Locate platelets.
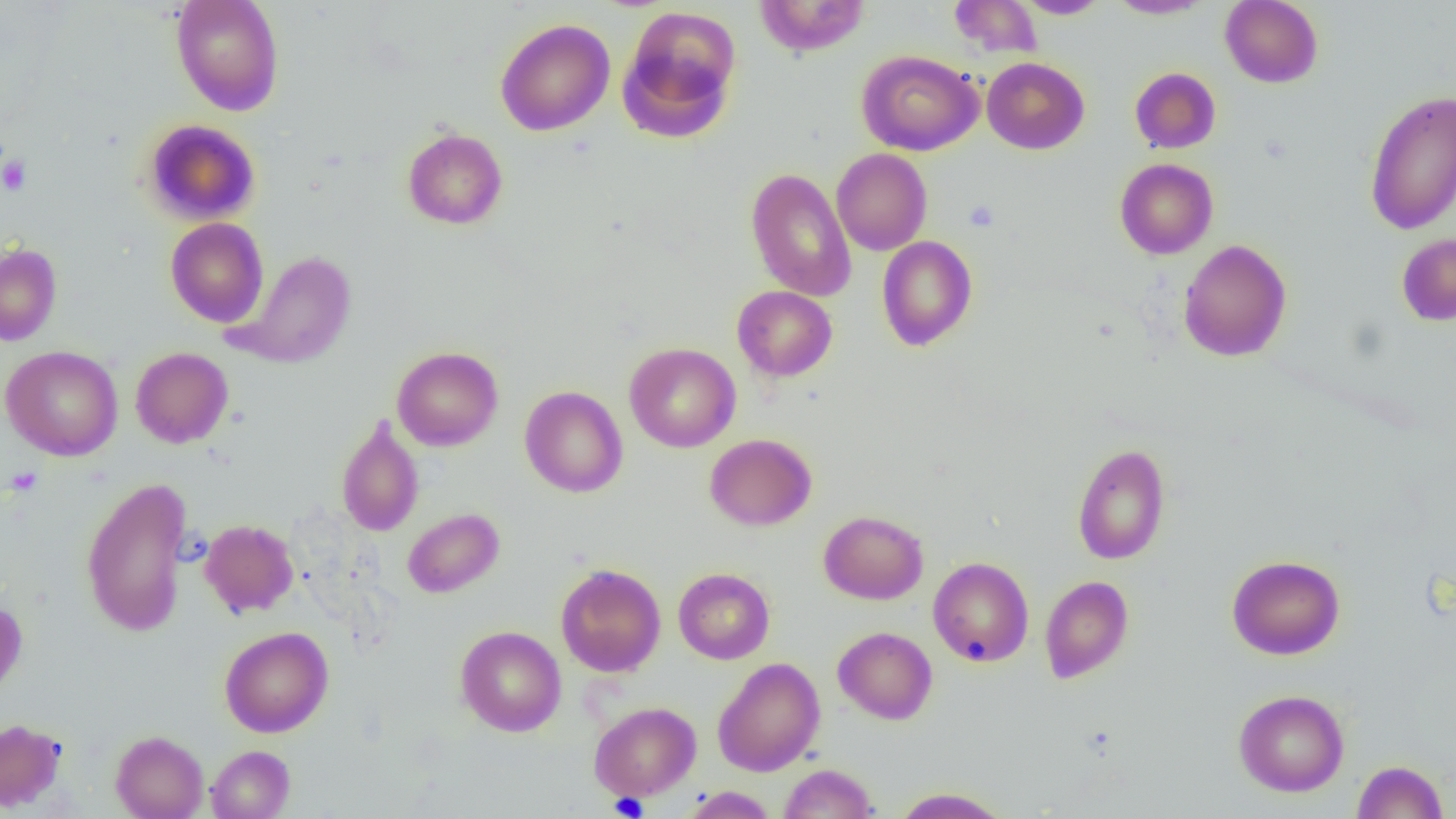

Approximate bounding boxes as named x1/y1/x2/y2 corners in pixels.
Platelets: (x1=0, y1=155, x2=31, y2=196), (x1=964, y1=200, x2=1000, y2=231), (x1=4, y1=466, x2=43, y2=496), (x1=610, y1=792, x2=649, y2=818).

Uninfected red blood cell locations: (x1=171, y1=0, x2=285, y2=116), (x1=755, y1=0, x2=870, y2=56), (x1=949, y1=0, x2=1043, y2=58), (x1=1106, y1=0, x2=1211, y2=19), (x1=1220, y1=0, x2=1323, y2=88), (x1=1015, y1=1, x2=1110, y2=18), (x1=618, y1=6, x2=743, y2=144), (x1=495, y1=18, x2=615, y2=136), (x1=856, y1=50, x2=983, y2=155), (x1=982, y1=57, x2=1089, y2=154), (x1=1130, y1=67, x2=1221, y2=153), (x1=1364, y1=89, x2=1456, y2=235), (x1=142, y1=118, x2=260, y2=225), (x1=402, y1=128, x2=508, y2=230), (x1=831, y1=148, x2=932, y2=255), (x1=1115, y1=158, x2=1218, y2=259), (x1=745, y1=167, x2=857, y2=302), (x1=165, y1=217, x2=269, y2=327), (x1=1397, y1=233, x2=1456, y2=325), (x1=877, y1=235, x2=978, y2=352), (x1=1178, y1=239, x2=1292, y2=362), (x1=0, y1=243, x2=62, y2=346), (x1=232, y1=250, x2=357, y2=369), (x1=732, y1=286, x2=837, y2=382), (x1=624, y1=342, x2=740, y2=452), (x1=1, y1=346, x2=124, y2=461), (x1=391, y1=346, x2=503, y2=451), (x1=130, y1=347, x2=233, y2=448), (x1=519, y1=385, x2=628, y2=498), (x1=336, y1=417, x2=424, y2=537), (x1=705, y1=434, x2=816, y2=531), (x1=1072, y1=444, x2=1171, y2=565), (x1=80, y1=476, x2=193, y2=637), (x1=403, y1=507, x2=504, y2=597), (x1=818, y1=510, x2=928, y2=604), (x1=200, y1=519, x2=299, y2=617), (x1=1227, y1=554, x2=1345, y2=659), (x1=928, y1=557, x2=1034, y2=667), (x1=556, y1=564, x2=666, y2=677), (x1=673, y1=567, x2=775, y2=664), (x1=1040, y1=575, x2=1134, y2=683), (x1=0, y1=600, x2=27, y2=699), (x1=455, y1=625, x2=566, y2=736), (x1=219, y1=626, x2=333, y2=737), (x1=833, y1=626, x2=938, y2=724), (x1=712, y1=657, x2=825, y2=777), (x1=1233, y1=689, x2=1349, y2=797), (x1=589, y1=701, x2=701, y2=800), (x1=0, y1=718, x2=66, y2=811), (x1=111, y1=730, x2=209, y2=819), (x1=206, y1=745, x2=295, y2=819), (x1=1352, y1=760, x2=1448, y2=819), (x1=779, y1=763, x2=877, y2=818), (x1=682, y1=786, x2=777, y2=818), (x1=891, y1=787, x2=1011, y2=818). Slide-level diagnosis: negative for blood parasites. 1000x magnification. Single field of view. Image is 1456×819 pixels. Light microscopy. Thin blood film.